Locate every Plasmodium parasite.
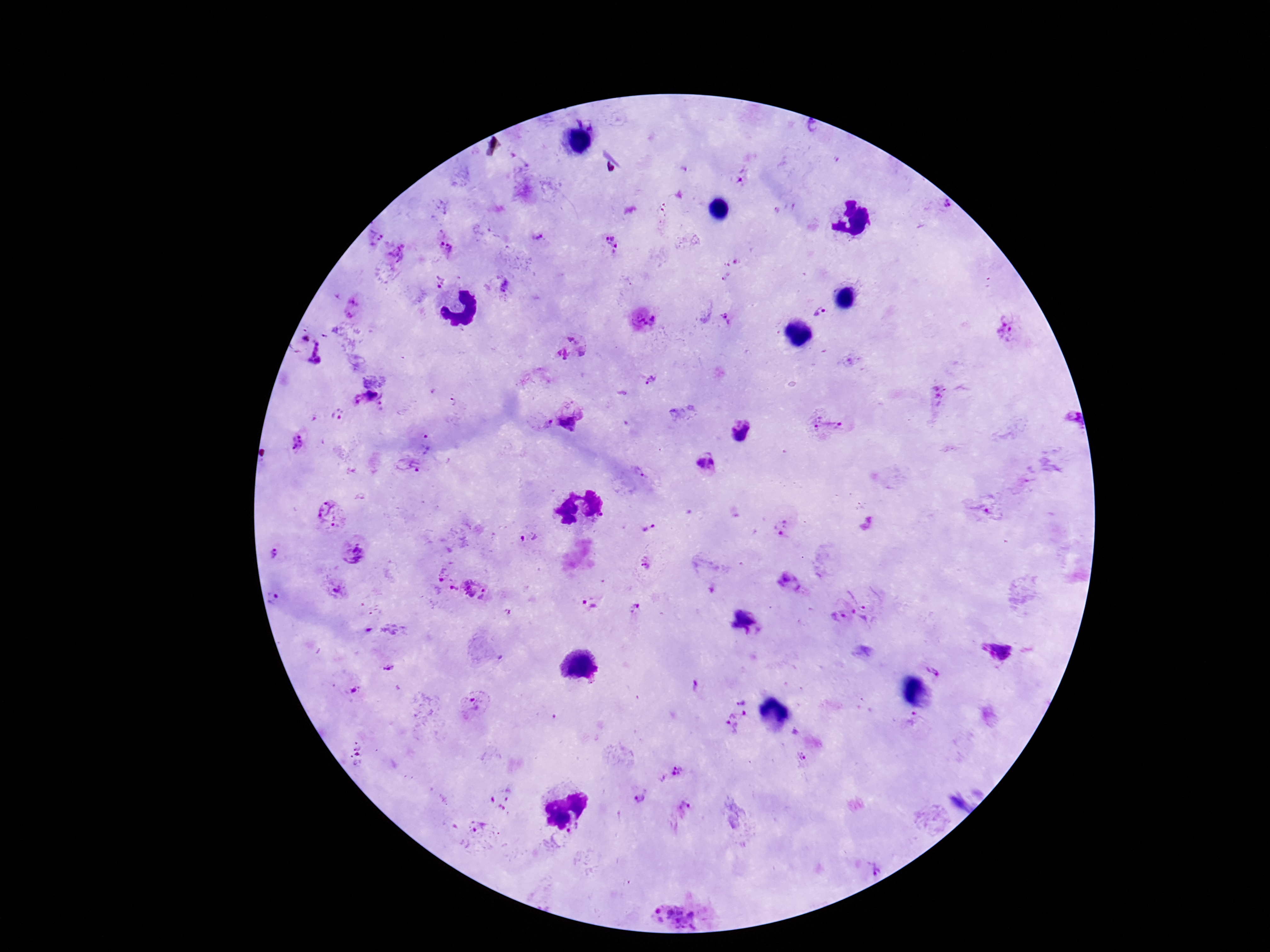

Approximate centers as (x, y) in pixels.
Plasmodium parasites: (812, 129), (743, 178), (942, 208), (375, 238), (539, 238), (610, 243), (446, 248), (399, 253), (439, 281), (501, 286), (352, 309), (823, 311), (727, 320), (644, 321), (1004, 335), (304, 338), (571, 347), (319, 354), (651, 380), (938, 399), (367, 401), (454, 401), (572, 412), (338, 414), (1066, 418), (539, 424), (827, 428), (741, 433), (300, 442), (428, 442), (704, 462), (407, 467), (641, 473), (981, 508), (331, 516), (782, 526), (649, 527), (530, 536), (354, 552), (274, 554), (647, 563), (440, 575), (790, 583), (334, 588), (452, 590), (475, 590), (868, 592), (276, 599), (591, 603), (635, 608), (834, 617), (859, 620), (391, 631), (996, 651), (935, 666), (390, 670), (354, 691), (741, 696), (474, 706), (737, 720), (912, 723), (359, 755), (801, 758), (680, 775), (637, 799), (500, 801), (685, 812), (477, 832), (680, 912).

Summary:
  - Capture: smartphone camera through the microscope eyepiece
  - Image size: 1270×952 pixels
  - Patient malaria status: infected
  - Magnification: 100x
  - Field of view: one from this slide
  - Preparation: thick blood smear
  - Stain: Giemsa